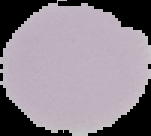
Summary:
  - Malaria status: uninfected
  - Image size: 151×136 pixels
  - Preparation: thin blood film
  - Image type: cell region segmented out of the field of view; surrounding area masked to black